Outline each uninfected red blood cell.
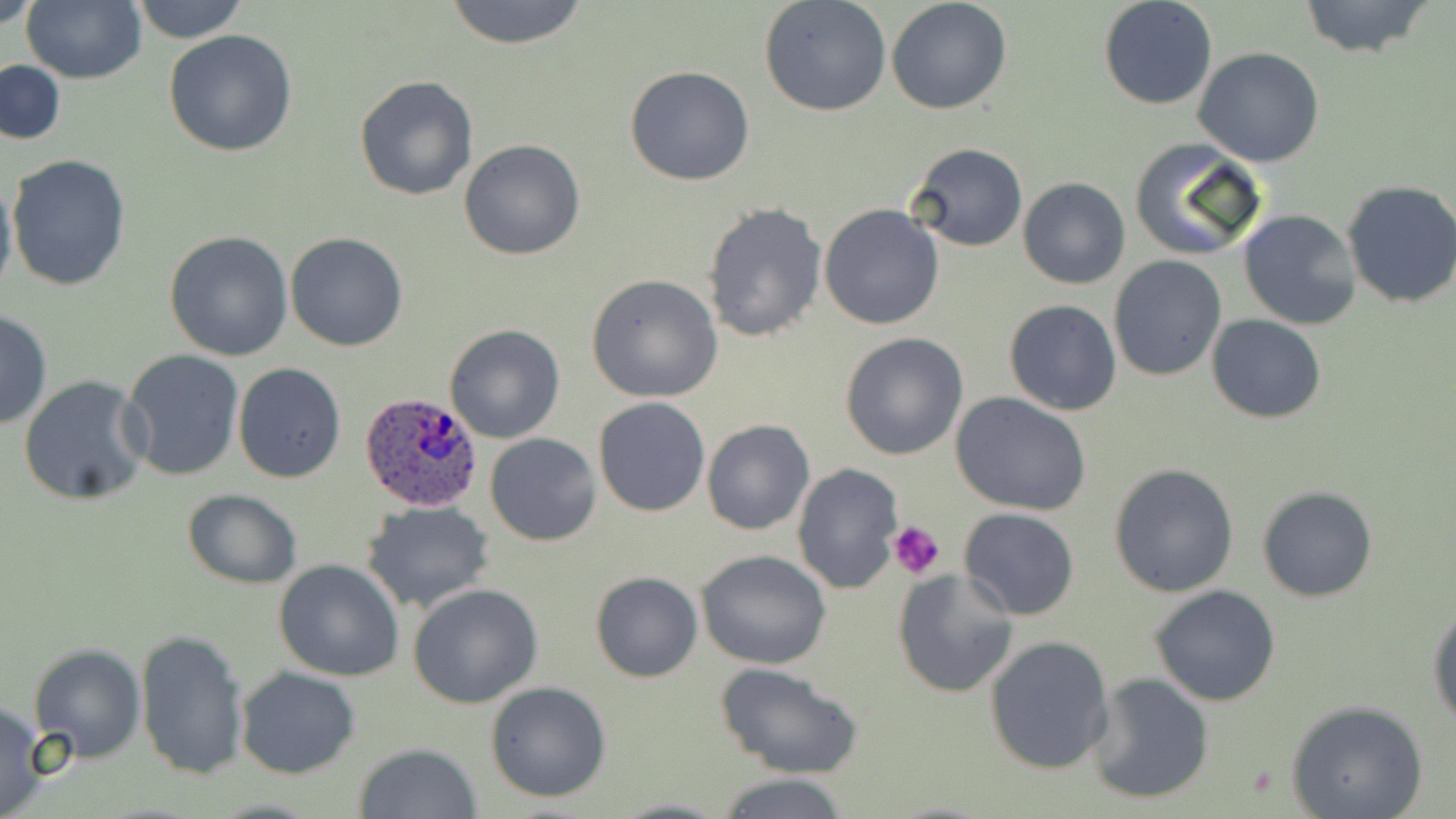

Approximate bounding boxes as (x1,y1)-(x2,y2) corner pairs in pixels.
Uninfected red blood cells: (2,0)-(40,31), (22,0)-(146,84), (129,0)-(252,44), (441,0)-(593,49), (759,0)-(891,118), (886,0)-(1013,115), (1098,0)-(1218,110), (1297,0)-(1438,59), (163,27)-(298,158), (1194,47)-(1325,167), (1,59)-(66,147), (624,65)-(755,186), (354,75)-(478,201), (1129,136)-(1270,262), (459,137)-(585,259), (908,142)-(1027,251), (4,153)-(131,292), (0,173)-(17,306), (1018,176)-(1131,288), (1341,179)-(1456,308), (702,202)-(827,344), (818,204)-(945,330), (1237,210)-(1362,330), (165,230)-(293,360), (285,232)-(410,351), (1108,255)-(1227,381), (584,275)-(723,403), (1005,301)-(1121,416), (1,309)-(51,432), (1207,315)-(1326,423), (444,323)-(565,443), (841,333)-(970,459), (119,348)-(244,482), (233,363)-(344,484), (17,376)-(152,505), (950,393)-(1093,516), (593,398)-(709,517), (701,419)-(814,536), (485,433)-(601,546), (1109,462)-(1238,597), (792,463)-(903,594), (1257,485)-(1378,602), (181,490)-(301,588), (362,502)-(495,612), (957,508)-(1081,622), (695,549)-(832,670), (273,558)-(405,681), (892,569)-(1018,696), (590,570)-(703,683), (407,583)-(543,708), (1150,584)-(1281,706), (1429,606)-(1456,731), (134,630)-(249,780), (983,635)-(1115,775), (28,643)-(146,762), (714,663)-(862,780), (236,667)-(361,779), (1088,673)-(1214,804), (485,680)-(613,802), (1286,699)-(1427,819), (0,700)-(47,819), (355,743)-(482,819), (712,772)-(856,818), (608,797)-(733,818).

Summary:
  - Platelet locations: (887,519)-(944,581)
  - Plasmodium ovale-infected red blood cell locations: (358,393)-(483,512)
  - Slide-level diagnosis: Plasmodium ovale
  - Field of view: single
  - Image size: 1456×819 pixels
  - Modality: light microscopy
  - Preparation: thin blood film
  - Stain: May-Grünwald-Giemsa
  - Magnification: 1000x